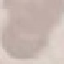
Malaria status: uninfected. Acquired by smartphone through the microscope eyepiece. Automatically extracted cell patch, resized to 64 × 64 pixels. Giemsa stain. Thin blood smear.